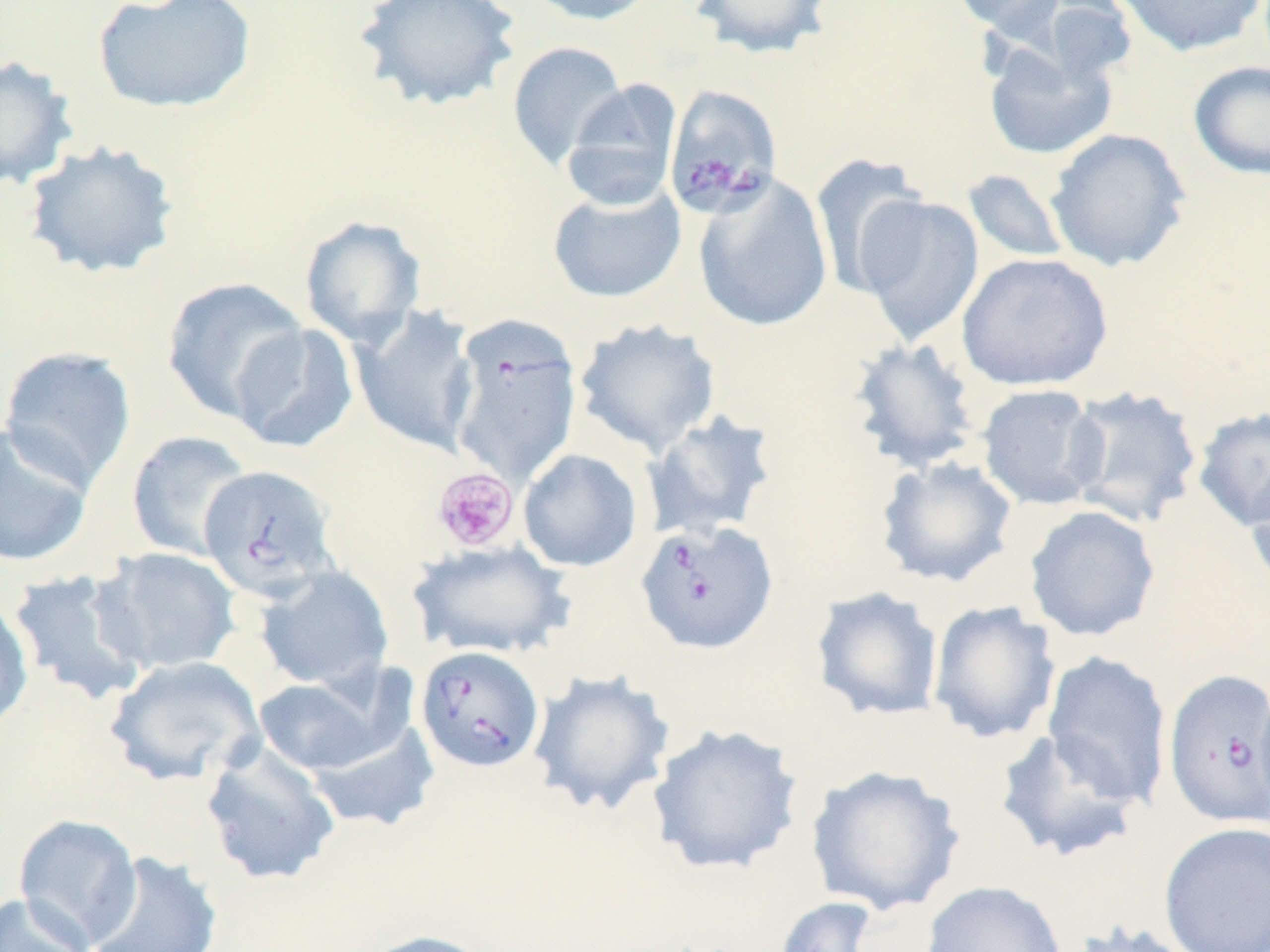

Summary:
  - Coordinate format: approximate bounding boxes as (x1, y1, x2, y2) in pixels
  - Platelet locations: (431, 467, 520, 553)
  - Babesia divergens-infected red blood cell locations: (663, 84, 783, 217), (448, 315, 582, 485), (199, 465, 341, 602), (634, 520, 778, 654), (415, 645, 545, 774), (1162, 669, 1270, 829)
  - Uninfected red blood cell locations: (92, 0, 258, 115), (520, 0, 660, 26), (688, 0, 836, 59), (947, 0, 1069, 37), (1112, 0, 1269, 58), (352, 1, 523, 111), (505, 40, 629, 169), (983, 42, 1118, 160), (0, 55, 80, 190), (1188, 60, 1270, 180), (561, 79, 683, 211), (1044, 128, 1191, 272), (22, 139, 180, 280), (810, 154, 929, 299), (962, 169, 1072, 264), (693, 174, 833, 333), (547, 183, 686, 303), (853, 195, 984, 346), (298, 215, 427, 348), (956, 252, 1114, 392), (160, 276, 309, 424), (350, 305, 481, 457), (574, 318, 722, 456), (228, 322, 359, 453), (847, 337, 982, 473), (0, 346, 137, 489), (976, 384, 1107, 510), (1063, 384, 1204, 528), (1192, 406, 1270, 532), (643, 410, 780, 542), (0, 423, 95, 569), (126, 430, 254, 562), (518, 448, 643, 572), (875, 456, 1018, 589), (1245, 457, 1270, 596), (1023, 505, 1161, 642), (408, 539, 573, 661), (95, 547, 242, 676), (254, 566, 394, 692), (5, 570, 152, 706), (810, 586, 944, 721), (0, 594, 34, 732), (927, 600, 1061, 745), (1041, 650, 1173, 808), (105, 655, 267, 788), (527, 668, 676, 817), (252, 672, 397, 776), (1253, 678, 1270, 827), (305, 720, 440, 833), (647, 722, 805, 876), (993, 728, 1145, 865), (199, 742, 341, 887), (805, 765, 965, 916), (12, 813, 143, 949), (1158, 821, 1270, 952), (84, 850, 223, 952), (920, 881, 1068, 952), (0, 892, 94, 952), (772, 896, 880, 952), (1065, 921, 1203, 952), (356, 929, 497, 952)
  - Slide-level diagnosis: Babesia divergens
  - Magnification: 1000x
  - Modality: optical microscopy
  - Stain: May-Grünwald-Giemsa
  - Preparation: thin blood film
  - Image size: 1270×952 pixels
  - Field of view: single